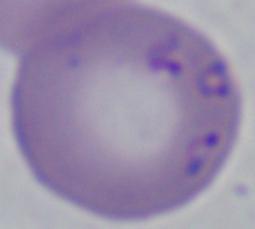
identification = Babesia
modality = photomicrograph
magnification = 1000x